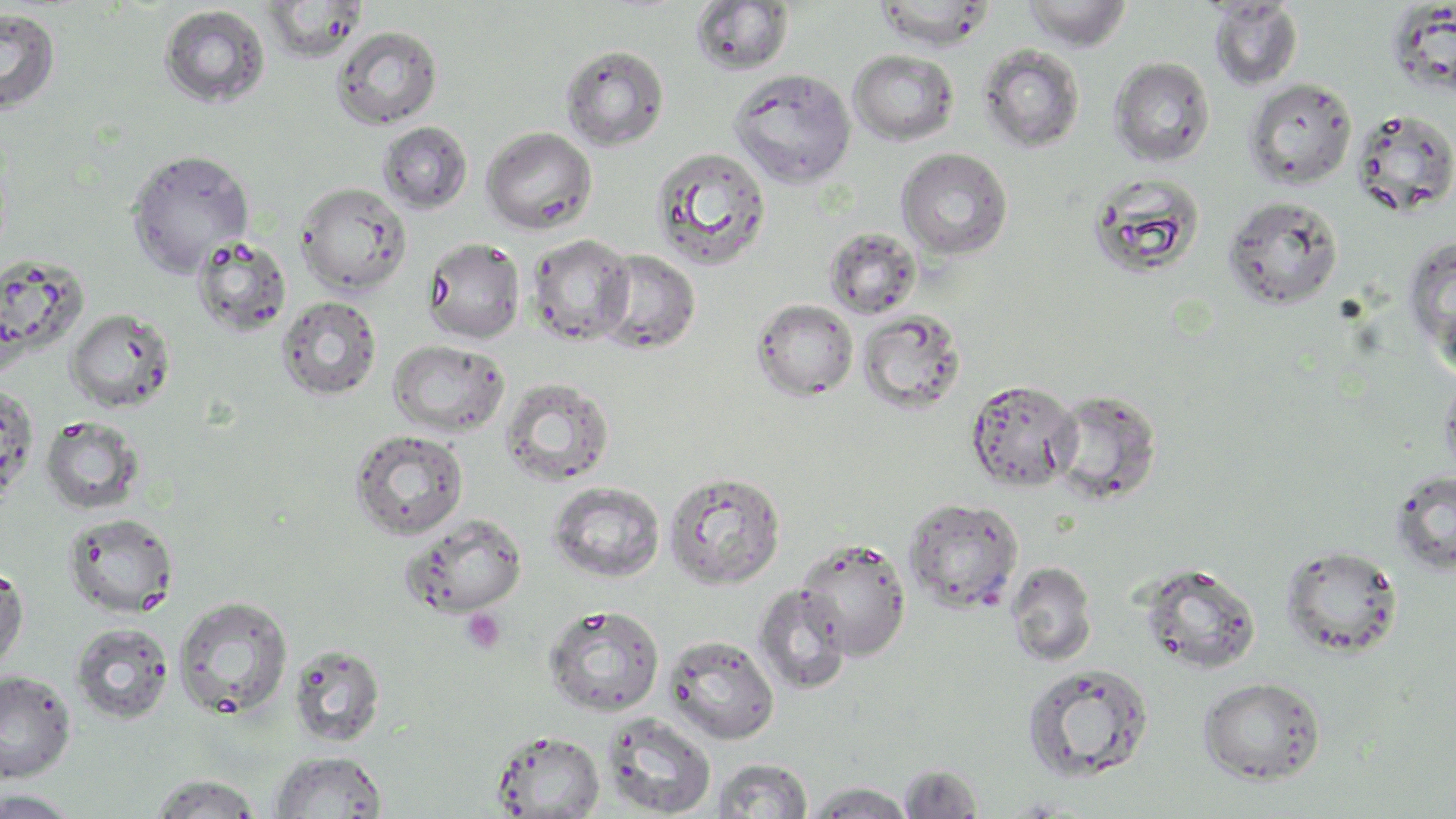

Summary:
  - Coordinate format: approximate bounding boxes as (x1, y1, x2, y2) in pixels
  - Uninfected red blood cell locations: (262, 0, 369, 62), (1020, 0, 1134, 51), (689, 1, 795, 76), (873, 1, 997, 51), (1207, 1, 1304, 90), (159, 4, 270, 109), (0, 8, 61, 115), (332, 26, 442, 129), (977, 44, 1085, 153), (560, 45, 669, 151), (848, 50, 960, 146), (1109, 57, 1216, 167), (729, 69, 857, 188), (1244, 78, 1357, 189), (1351, 108, 1456, 217), (378, 121, 474, 214), (481, 127, 597, 234), (650, 147, 771, 271), (896, 148, 1013, 260), (125, 149, 255, 275), (1086, 171, 1207, 280), (296, 182, 412, 295), (1222, 194, 1344, 310), (824, 228, 921, 318), (525, 233, 634, 346), (191, 235, 292, 337), (1402, 236, 1456, 367), (422, 237, 525, 343), (594, 249, 701, 354), (1, 253, 90, 364), (277, 295, 381, 401), (752, 298, 858, 400), (66, 308, 176, 413), (858, 309, 966, 414), (387, 339, 510, 437), (1439, 371, 1456, 487), (499, 377, 616, 488), (965, 379, 1081, 493), (0, 381, 39, 504), (1049, 389, 1163, 505), (40, 415, 145, 515), (349, 429, 469, 540), (1390, 469, 1456, 577), (663, 471, 785, 589), (548, 482, 666, 583), (902, 497, 1024, 613), (62, 513, 179, 618), (399, 514, 529, 617), (795, 538, 912, 659), (1279, 544, 1403, 659), (1006, 561, 1098, 666), (0, 562, 28, 674), (1137, 563, 1261, 674), (752, 583, 852, 695), (173, 595, 294, 720), (543, 604, 664, 717), (70, 623, 173, 723), (664, 635, 780, 744), (288, 643, 386, 748), (1021, 663, 1154, 783), (0, 670, 76, 782), (1197, 676, 1325, 785), (600, 712, 717, 818), (491, 730, 605, 817), (270, 751, 388, 818), (713, 758, 813, 817), (899, 763, 984, 818), (147, 773, 264, 818), (806, 782, 915, 817), (0, 789, 82, 817)
  - Platelet locations: (461, 607, 507, 655)
  - Slide-level diagnosis: no evidence of blood parasites
  - Preparation: thin blood film
  - Field of view: single
  - Stain: May-Grünwald-Giemsa
  - Image size: 1456×819 pixels
  - Modality: light microscopy
  - Magnification: 1000x